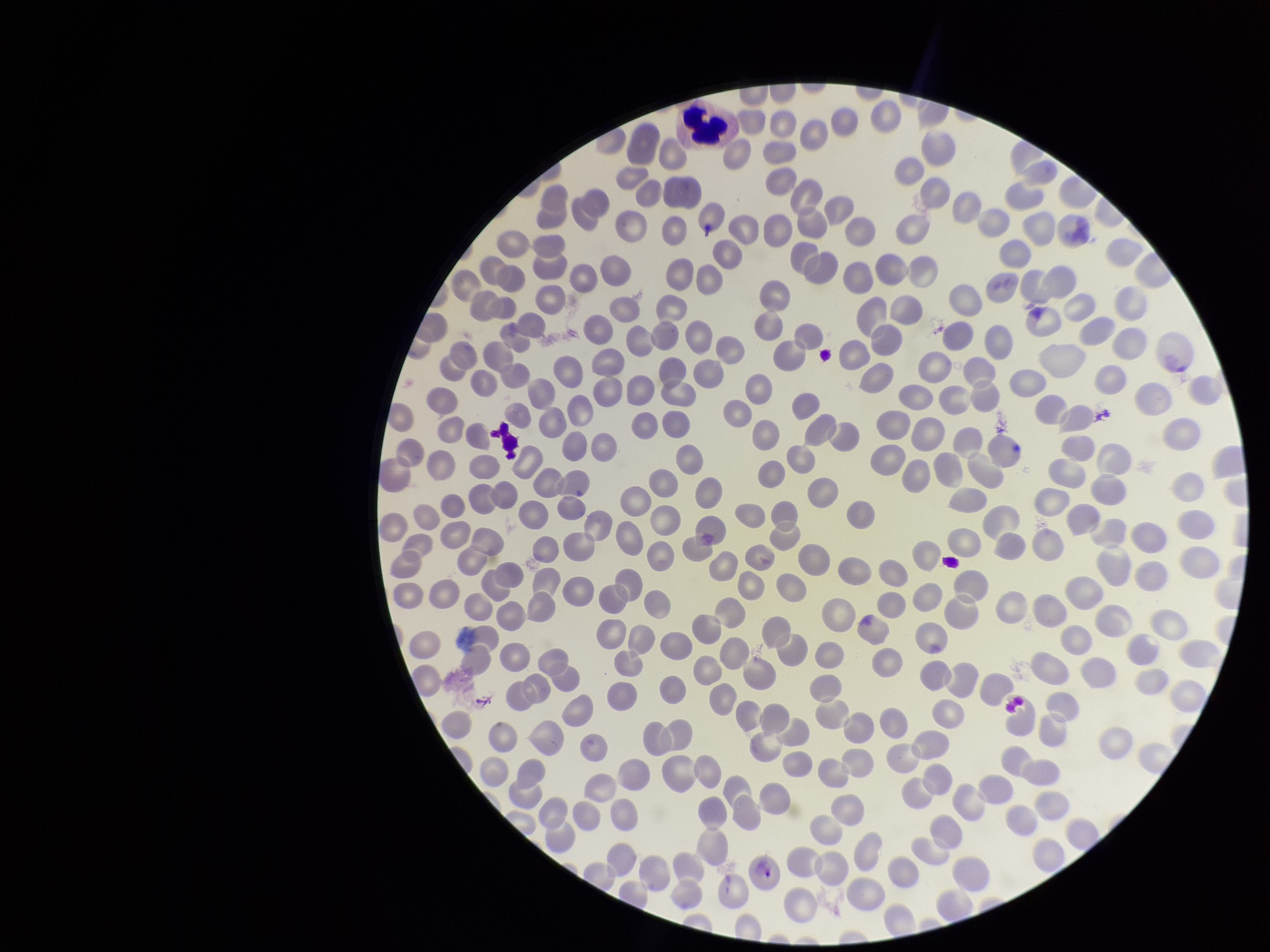
Summary:
  - Image size: 1270×952 pixels
  - Parasitized red blood cell count: 0
  - Capture: smartphone photograph through the microscope eyepiece
  - Field of view: single
  - Preparation: thin smear
  - Red blood cell count: 285
  - Stain: Giemsa
  - Parasitized red blood cells: none identified
  - Patient malaria status: negative